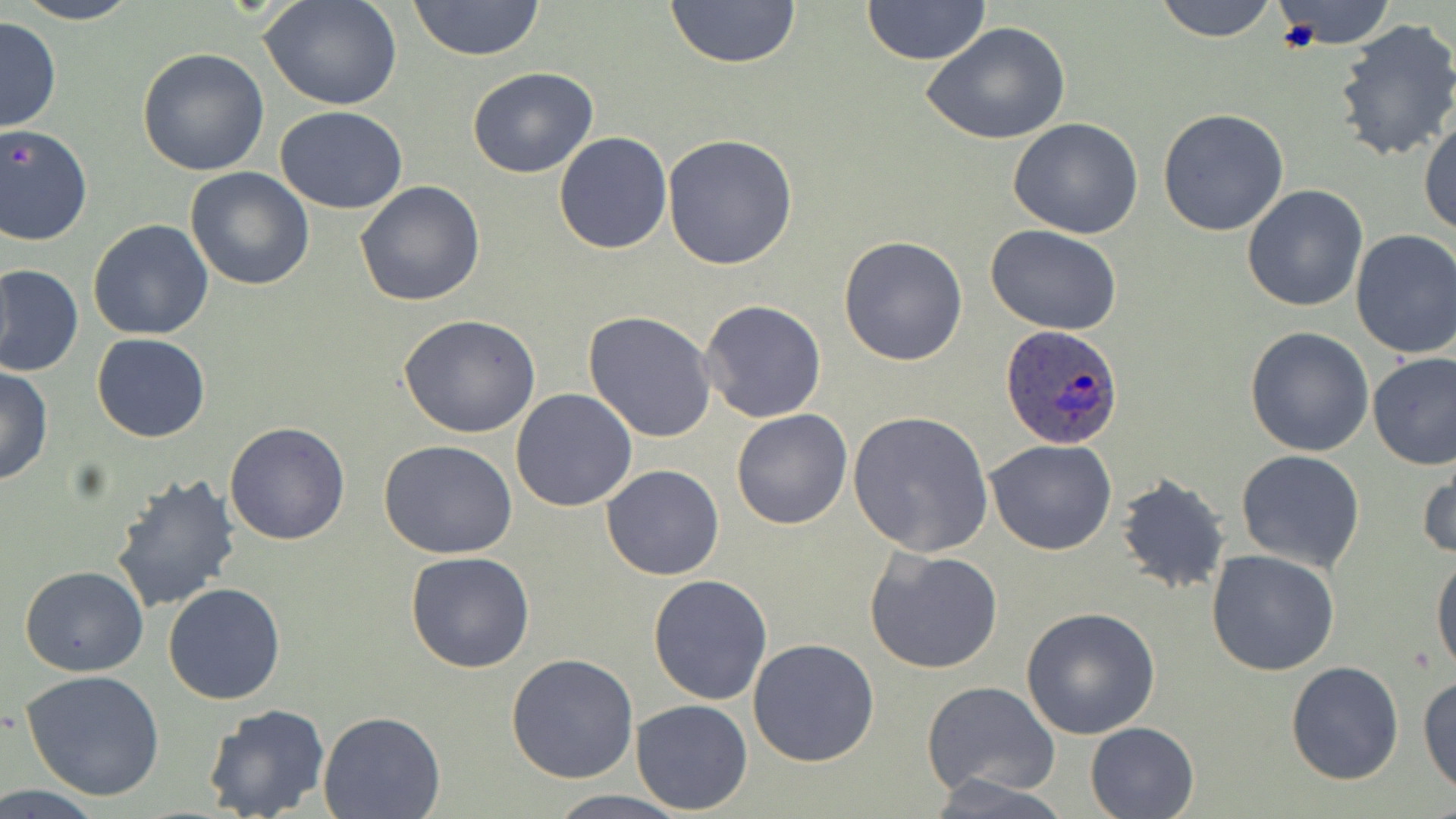

Summary:
  - Coordinate format: approximate bounding boxes as (x1, y1, x2, y2) in pixels
  - Plasmodium ovale-infected red blood cell locations: (999, 326, 1126, 450)
  - Uninfected red blood cell locations: (10, 0, 146, 25), (662, 0, 804, 70), (862, 0, 989, 65), (1153, 0, 1279, 43), (1267, 0, 1402, 50), (258, 1, 405, 111), (407, 1, 547, 60), (0, 14, 61, 135), (1331, 16, 1456, 164), (922, 21, 1071, 145), (138, 46, 271, 176), (467, 66, 598, 179), (275, 106, 407, 213), (1157, 108, 1290, 236), (1419, 113, 1456, 239), (1008, 119, 1145, 239), (0, 124, 93, 246), (553, 132, 673, 255), (663, 133, 799, 269), (185, 166, 315, 291), (355, 180, 486, 307), (1241, 185, 1369, 313), (87, 219, 215, 339), (985, 223, 1123, 335), (1350, 230, 1456, 359), (838, 235, 968, 366), (0, 264, 84, 378), (698, 299, 828, 424), (583, 311, 716, 444), (399, 313, 544, 440), (1244, 327, 1375, 457), (91, 334, 211, 442), (1367, 352, 1456, 471), (0, 366, 53, 487), (511, 388, 638, 513), (732, 410, 853, 529), (846, 412, 994, 558), (224, 421, 351, 545), (984, 438, 1117, 556), (379, 439, 518, 559), (1236, 449, 1366, 573), (1417, 452, 1456, 565), (601, 465, 725, 581), (110, 473, 243, 615), (1114, 473, 1232, 594), (864, 548, 1003, 675), (1206, 548, 1340, 677), (1430, 551, 1456, 676), (404, 552, 536, 673), (20, 567, 147, 677), (647, 573, 774, 705), (163, 583, 286, 704), (1020, 606, 1162, 740), (747, 638, 880, 767), (506, 651, 639, 784), (1285, 660, 1404, 785), (20, 670, 166, 799), (1418, 673, 1456, 795), (920, 680, 1063, 801), (631, 699, 752, 815), (202, 703, 332, 819), (318, 712, 445, 819), (1084, 721, 1201, 818), (929, 775, 1073, 817), (541, 791, 695, 819)
  - Platelet locations: (1275, 16, 1323, 55), (9, 144, 35, 171)
  - Slide-level diagnosis: Plasmodium ovale
  - Preparation: thin blood smear
  - Stain: May-Grünwald-Giemsa
  - Field of view: one of a larger specimen
  - Magnification: 1000x
  - Image size: 1456×819 pixels
  - Modality: optical microscopy